Give the extent of all Plasmodium vivax-infected red blood cells.
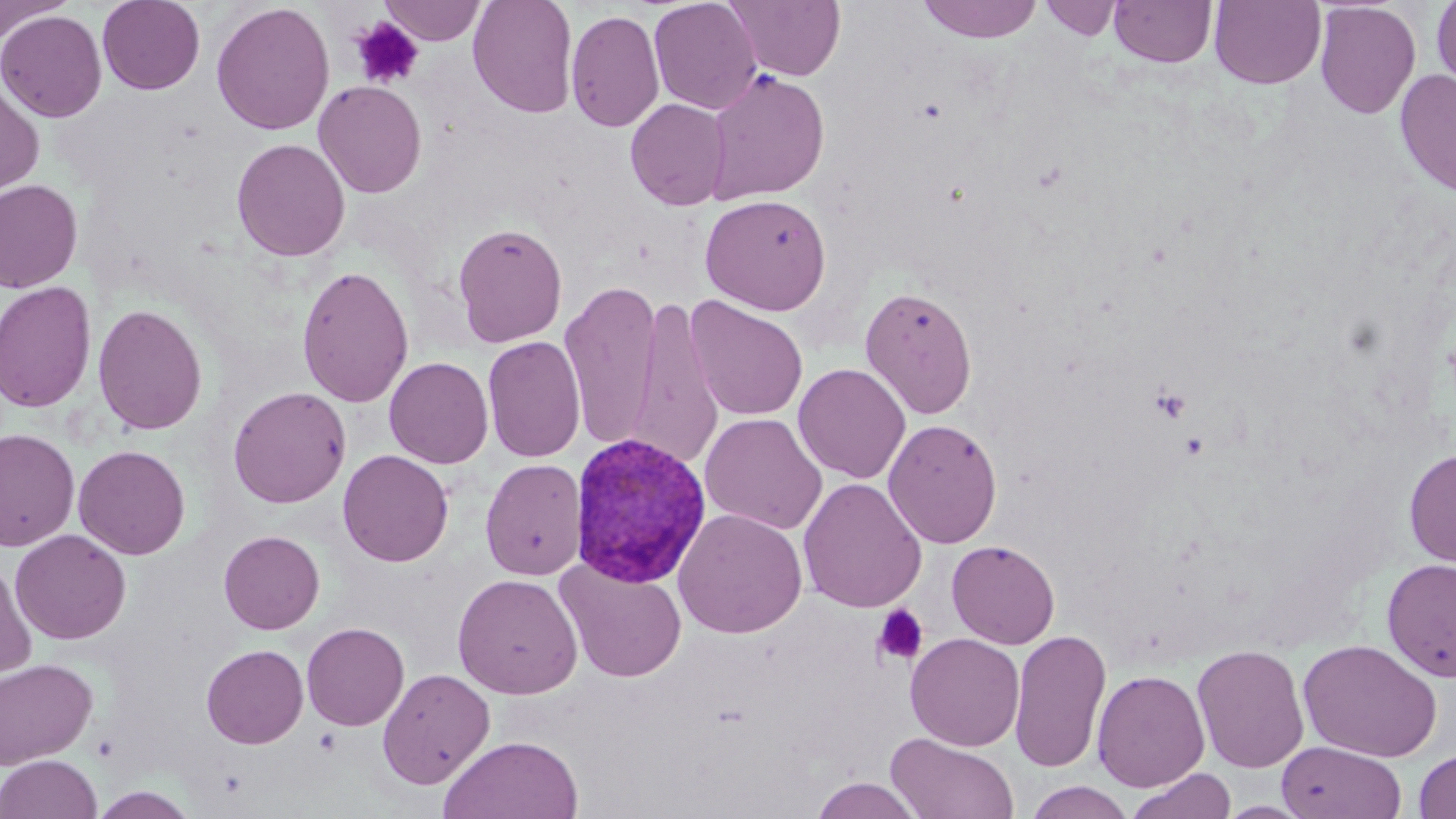
Approximate bounding boxes as [x1, y1, x2, y2] in pixels.
Plasmodium vivax-infected red blood cells: [568, 432, 712, 587].

Platelet locations: [350, 17, 424, 89], [1151, 387, 1192, 423], [1180, 430, 1209, 459], [872, 604, 929, 666]. Uninfected red blood cell locations: [97, 0, 205, 95], [379, 0, 487, 45], [468, 0, 578, 118], [648, 0, 762, 115], [727, 0, 845, 81], [918, 0, 1042, 43], [1039, 0, 1123, 41], [1109, 0, 1217, 68], [1209, 0, 1326, 89], [1431, 0, 1456, 96], [1314, 1, 1421, 118], [0, 2, 71, 43], [211, 2, 335, 136], [566, 9, 665, 133], [0, 10, 107, 123], [1394, 68, 1456, 197], [704, 69, 830, 205], [0, 80, 44, 196], [313, 80, 427, 198], [625, 98, 731, 211], [231, 137, 350, 262], [0, 179, 83, 293], [700, 193, 832, 315], [452, 222, 567, 347], [296, 264, 414, 408], [559, 279, 662, 451], [0, 281, 97, 413], [859, 284, 978, 420], [627, 294, 725, 472], [685, 296, 808, 422], [93, 304, 208, 436], [482, 335, 586, 463], [384, 356, 494, 468], [792, 363, 911, 484], [228, 386, 351, 508], [700, 413, 827, 535], [883, 418, 1003, 548], [0, 427, 80, 551], [73, 444, 191, 560], [1403, 447, 1456, 567], [338, 450, 454, 567], [480, 458, 587, 581], [798, 478, 927, 613], [673, 508, 807, 639], [10, 529, 131, 645], [218, 530, 325, 634], [947, 539, 1060, 649], [1381, 557, 1456, 682], [554, 558, 688, 683], [0, 561, 37, 682], [452, 573, 583, 699], [302, 622, 409, 731], [1009, 628, 1112, 774], [905, 633, 1024, 751], [1297, 638, 1443, 762], [1191, 643, 1310, 773], [201, 644, 309, 749], [0, 658, 98, 770], [377, 667, 495, 789], [1092, 669, 1210, 792], [886, 733, 1019, 818], [440, 734, 583, 819], [1276, 740, 1407, 819], [1414, 749, 1456, 819], [0, 754, 102, 819], [1126, 769, 1237, 819], [809, 777, 926, 818], [1024, 781, 1135, 818], [88, 787, 199, 819]. Slide-level diagnosis: Plasmodium vivax. Single field of view. Image is 1456×819 pixels. 1000x magnification. May-Grünwald-Giemsa-stained preparation. Optical microscopy. Thin blood smear.